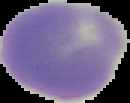

Malaria status: uninfected. Image is 130×103 pixels. Cell region segmented out of the field of view; the surrounding area is masked to black. From a thin blood film.